Describe the morphology of the red blood cells.
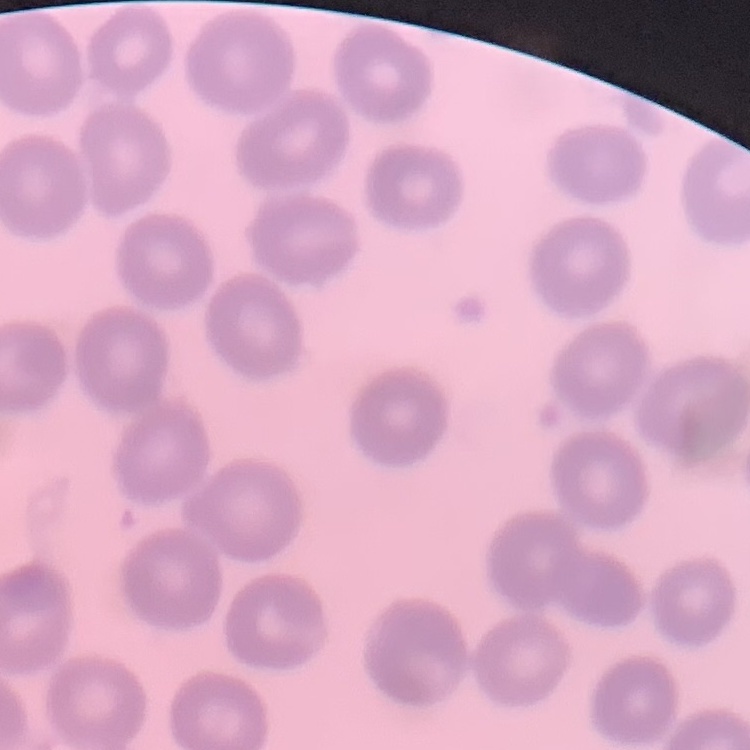
No rouleaux formation.

Thin blood film. One tile cut from a larger photomicrograph. Stained with either Field's or Giemsa.